Identify the cell.
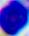

A leukocyte.

modality = micrograph
magnification = 400x